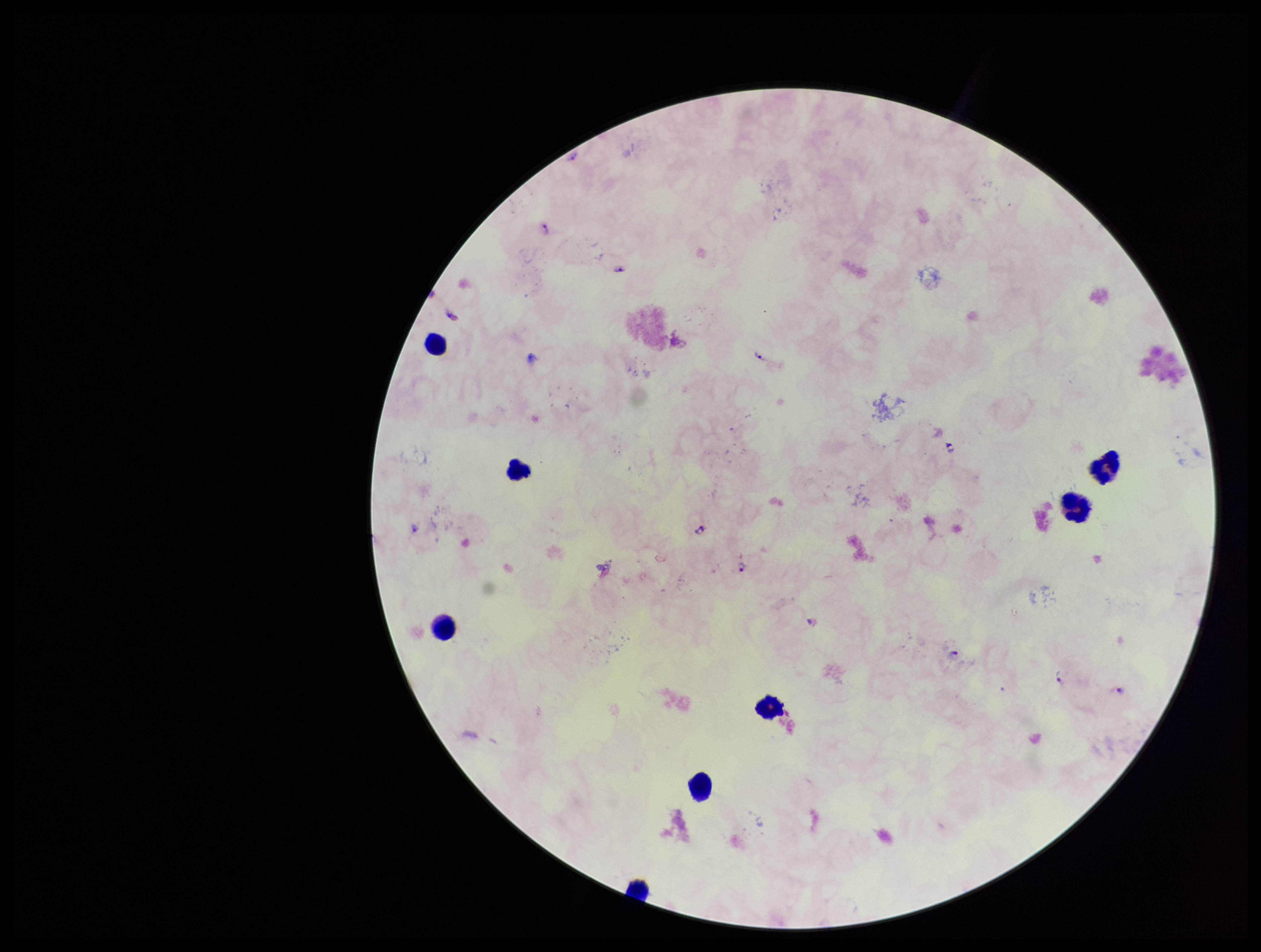
Summary:
  - Capture: smartphone photograph through the microscope eyepiece
  - Parasite count: 10
  - Image size: 1261×952 pixels
  - Patient malaria status: positive
  - Species reported for this patient: Plasmodium falciparum
  - Plasmodium parasites: identified
  - Leukocyte count: 8
  - Field of view: single
  - Preparation: thick
  - Stain: Giemsa